Outline each blood parasite and name the species.
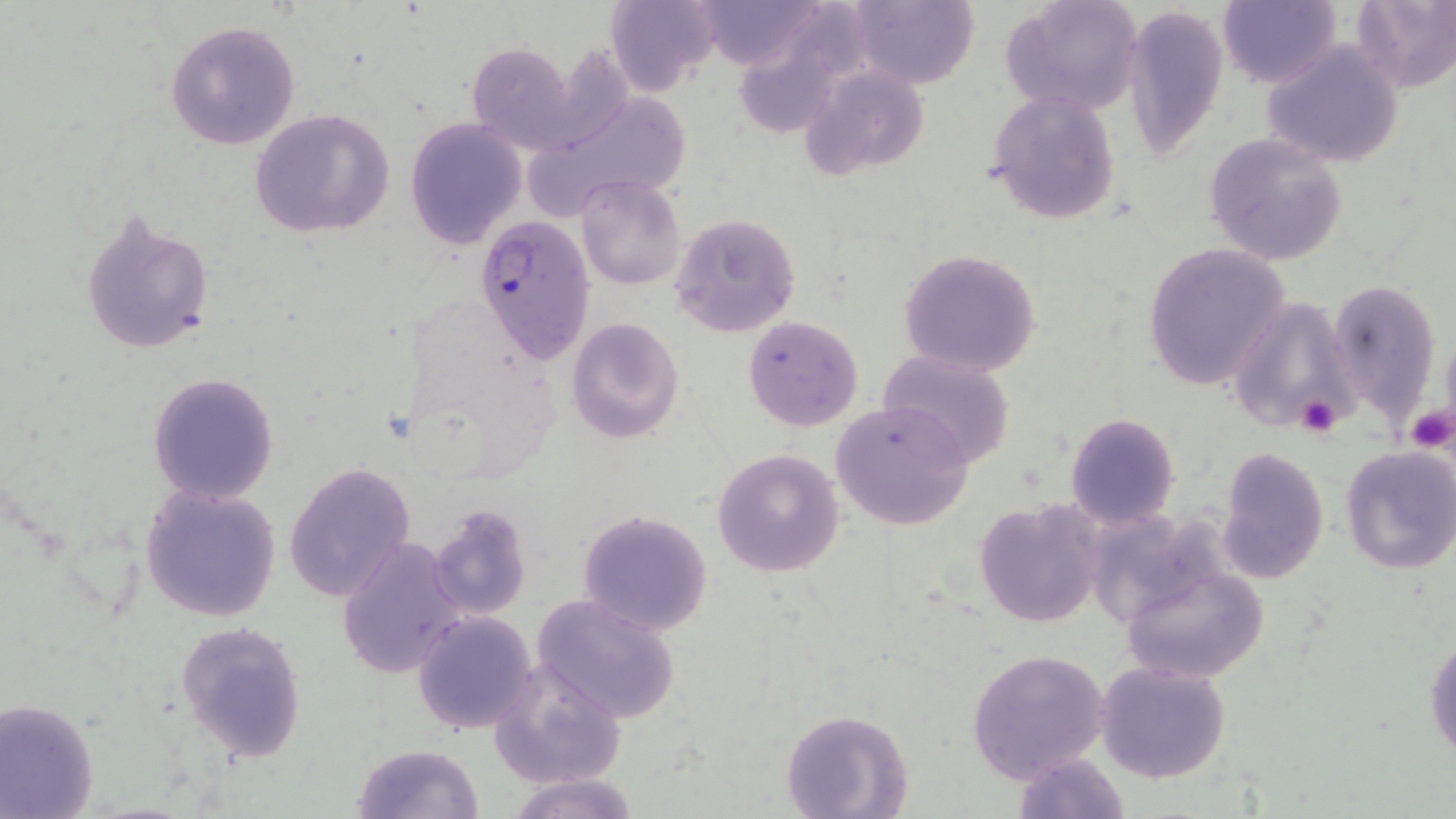

Approximate bounding boxes as [x1, y1, x2, y2] in pixels.
Plasmodium falciparum-infected red blood cells: [473, 214, 595, 366].
No Plasmodium ovale, Plasmodium malariae, Plasmodium vivax, Babesia divergens, or Trypanosoma brucei observed.

slide-level diagnosis = Plasmodium falciparum
magnification = 1000x
modality = optical microscopy
uninfected red blood cell locations = approximate bounding boxes as [x1, y1, x2, y2] in pixels: [694, 0, 829, 70], [851, 0, 980, 90], [1002, 0, 1145, 118], [1219, 0, 1342, 89], [607, 1, 721, 96], [1351, 1, 1456, 91], [1125, 5, 1227, 158], [166, 21, 299, 151], [1262, 39, 1406, 168], [466, 42, 577, 155], [801, 67, 932, 183], [987, 89, 1122, 223], [520, 93, 692, 223], [248, 109, 396, 239], [404, 117, 527, 249], [1203, 131, 1351, 267], [576, 176, 686, 292], [78, 208, 214, 356], [671, 212, 801, 339], [1142, 243, 1290, 390], [898, 248, 1041, 377], [1329, 278, 1443, 423], [1231, 298, 1358, 429], [742, 316, 864, 431], [566, 317, 683, 443], [878, 347, 1017, 467], [147, 372, 279, 504], [830, 400, 974, 532], [1064, 413, 1179, 530], [1339, 445, 1455, 575], [1216, 446, 1330, 586], [712, 448, 845, 578], [285, 461, 416, 603], [141, 483, 280, 622], [974, 497, 1105, 629], [427, 502, 533, 620], [577, 509, 713, 637], [336, 536, 465, 680], [1116, 559, 1269, 684], [532, 592, 682, 725], [413, 610, 538, 734], [176, 622, 307, 762], [1426, 632, 1456, 764], [966, 648, 1110, 782], [488, 657, 627, 790], [1094, 662, 1232, 784], [0, 699, 100, 818], [782, 708, 911, 817], [352, 744, 484, 819], [1011, 749, 1130, 819], [506, 772, 637, 818]
stain = May-Grünwald-Giemsa
preparation = thin blood film
platelet locations = approximate bounding boxes as [x1, y1, x2, y2] in pixels: [1295, 393, 1345, 435], [1406, 403, 1455, 452]
field of view = single
image size = 1456×819 pixels